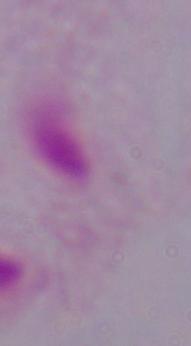

1000x magnification. A trichomonad is shown. Micrograph.